Assess this cell for malaria.
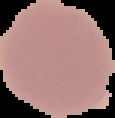

It is uninfected.

Cell region segmented out of the field of view; the surrounding area is masked to black. Image is 115×118 pixels. From a thin blood film.